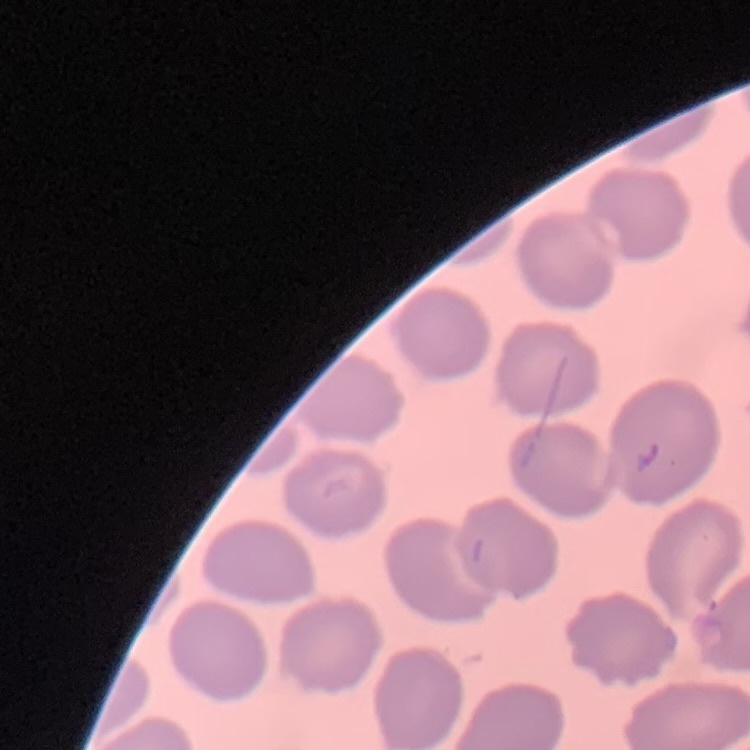
{
  "erythrocyte_morphology": "no rouleaux formation",
  "preparation": "thin blood smear",
  "image_type": "square crop of a larger photomicrograph",
  "stain": "Field's or Giemsa"
}